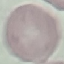

Result: no malaria parasites seen. Automatically extracted cell patch, resized to 64 × 64 pixels. Giemsa stain. Thin smear of blood. Acquired by smartphone through the microscope eyepiece.